Outline platelets.
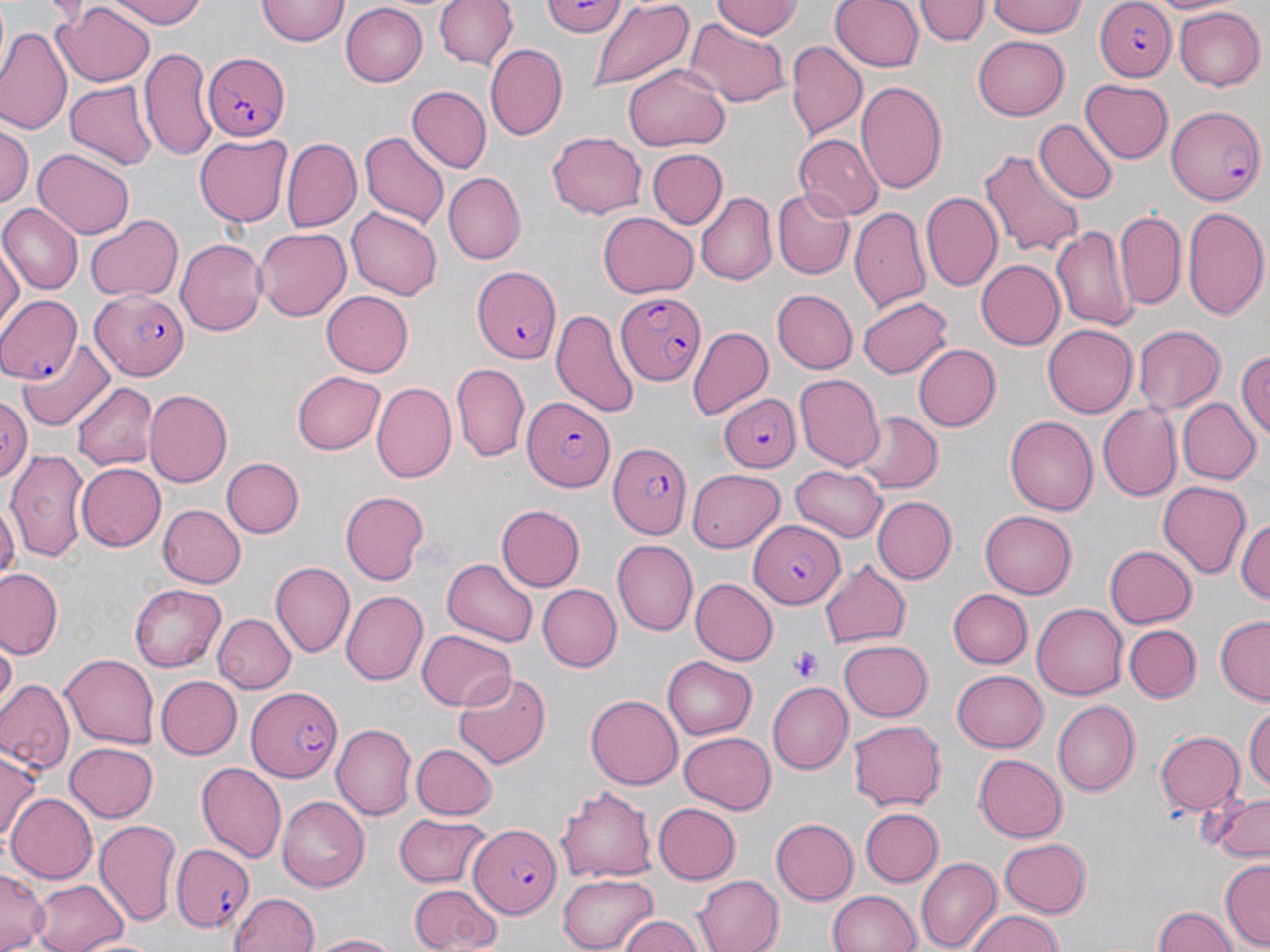
Approximate bounding boxes as (x1, y1, x2, y2) in pixels.
Platelets: (791, 646, 823, 680).

Uninfected red blood cell locations: (101, 0, 211, 28), (257, 0, 349, 46), (433, 0, 517, 73), (538, 0, 629, 40), (712, 0, 799, 40), (830, 0, 924, 73), (915, 0, 987, 46), (987, 0, 1087, 38), (1155, 0, 1235, 17), (584, 2, 695, 94), (340, 3, 429, 86), (53, 4, 156, 88), (983, 4, 1082, 79), (1173, 6, 1266, 90), (679, 19, 792, 107), (2, 25, 71, 134), (972, 34, 1070, 120), (787, 42, 866, 138), (486, 44, 567, 140), (140, 47, 213, 162), (623, 66, 730, 149), (855, 79, 947, 197), (1081, 79, 1174, 165), (64, 81, 156, 169), (408, 85, 492, 172), (1032, 119, 1115, 205), (2, 123, 32, 215), (361, 132, 448, 229), (546, 132, 646, 219), (196, 133, 291, 225), (791, 133, 882, 220), (281, 140, 362, 232), (647, 148, 728, 231), (35, 149, 134, 238), (979, 149, 1084, 260), (442, 173, 526, 265), (772, 188, 855, 278), (697, 190, 776, 284), (919, 192, 1001, 292), (0, 205, 81, 294), (1183, 205, 1269, 322), (850, 206, 930, 313), (346, 207, 442, 301), (1115, 211, 1186, 312), (85, 213, 184, 302), (599, 213, 698, 299), (253, 226, 353, 322), (1050, 226, 1134, 332), (177, 240, 264, 338), (0, 244, 23, 335), (976, 260, 1065, 348), (772, 290, 857, 374), (321, 292, 414, 377), (858, 296, 954, 378), (551, 305, 640, 417), (1132, 324, 1225, 415), (1042, 325, 1135, 418), (688, 326, 773, 420), (19, 339, 116, 430), (914, 344, 1001, 431), (1234, 349, 1270, 442), (451, 365, 529, 460), (292, 370, 386, 454), (794, 374, 883, 470), (73, 381, 158, 471), (372, 381, 456, 483), (143, 390, 232, 487), (0, 395, 29, 487), (1176, 398, 1259, 484), (1097, 404, 1182, 500), (853, 411, 940, 493), (1004, 416, 1097, 515), (6, 448, 90, 563), (221, 456, 303, 537), (74, 460, 165, 549), (790, 463, 886, 541), (690, 466, 786, 552), (1156, 481, 1253, 579), (340, 491, 429, 585), (4, 492, 32, 584), (1216, 494, 1267, 594), (0, 496, 18, 590), (871, 496, 955, 584), (157, 503, 246, 586), (495, 504, 584, 592), (979, 511, 1074, 599), (1236, 514, 1270, 608), (613, 540, 697, 634), (1104, 545, 1196, 629), (441, 559, 538, 647), (819, 560, 912, 646), (270, 562, 354, 658), (0, 567, 61, 657), (692, 579, 777, 666), (131, 583, 227, 672), (536, 583, 620, 673), (948, 588, 1033, 669), (340, 590, 428, 685), (1033, 603, 1127, 700), (214, 614, 296, 694), (1214, 617, 1269, 704), (1124, 623, 1200, 703), (417, 627, 518, 710), (838, 639, 933, 720), (2, 643, 19, 712), (61, 654, 158, 748), (662, 656, 757, 739), (952, 669, 1048, 751), (453, 670, 550, 767), (156, 676, 241, 759), (0, 678, 75, 776), (768, 683, 852, 773), (586, 693, 683, 789), (1053, 699, 1139, 796), (1244, 703, 1270, 793), (847, 718, 946, 810), (331, 723, 415, 821), (1155, 730, 1244, 817), (678, 733, 776, 813), (66, 740, 160, 821), (411, 743, 497, 819), (0, 752, 40, 850), (974, 754, 1067, 841), (195, 761, 287, 863), (556, 783, 659, 881), (1202, 789, 1270, 862), (6, 793, 97, 884), (276, 795, 367, 890), (653, 804, 740, 883), (859, 807, 941, 888), (392, 812, 490, 888), (94, 818, 181, 925), (772, 819, 859, 902), (999, 838, 1092, 916), (916, 855, 1001, 950), (1219, 859, 1270, 948), (1, 868, 49, 951), (558, 873, 661, 949), (693, 875, 783, 952), (29, 877, 130, 952), (407, 882, 500, 951), (827, 889, 922, 952), (229, 890, 321, 952), (966, 908, 1067, 952), (1151, 908, 1239, 952), (615, 914, 706, 952), (309, 932, 408, 951), (78, 934, 165, 952). Plasmodium falciparum-infected red blood cell locations: (1092, 0, 1177, 82), (201, 53, 290, 140), (1166, 105, 1266, 204), (471, 265, 561, 362), (616, 290, 704, 386), (89, 291, 192, 381), (0, 294, 85, 389), (717, 392, 801, 471), (521, 394, 613, 491), (604, 437, 687, 540), (748, 521, 845, 609), (247, 684, 342, 783), (468, 820, 561, 918), (171, 845, 256, 932). Slide-level diagnosis: Plasmodium falciparum. May-Grünwald-Giemsa-stained preparation. Thin blood film. Single field of view. Optical microscopy. 1000x magnification. Image is 1270×952 pixels.